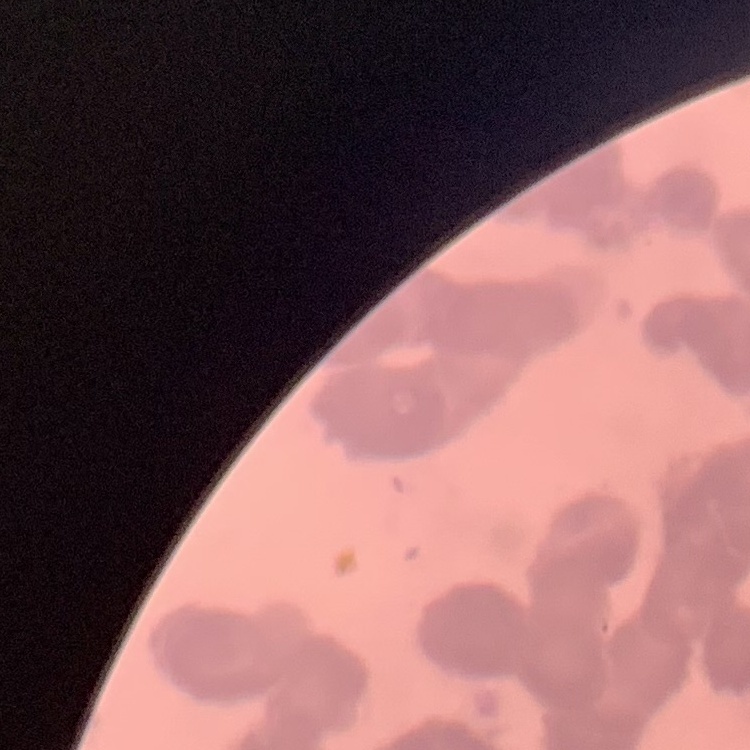
Summary:
  - Red blood cell morphology: rouleaux formation
  - Stain: Field's or Giemsa
  - Image type: square crop of a larger photomicrograph
  - Preparation: thin blood smear